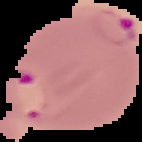

malaria status = parasitized
image size = 142×142 pixels
preparation = thin blood smear
image type = cell region segmented out of the field of view; surrounding area masked to black